Locate every uninfected red blood cell.
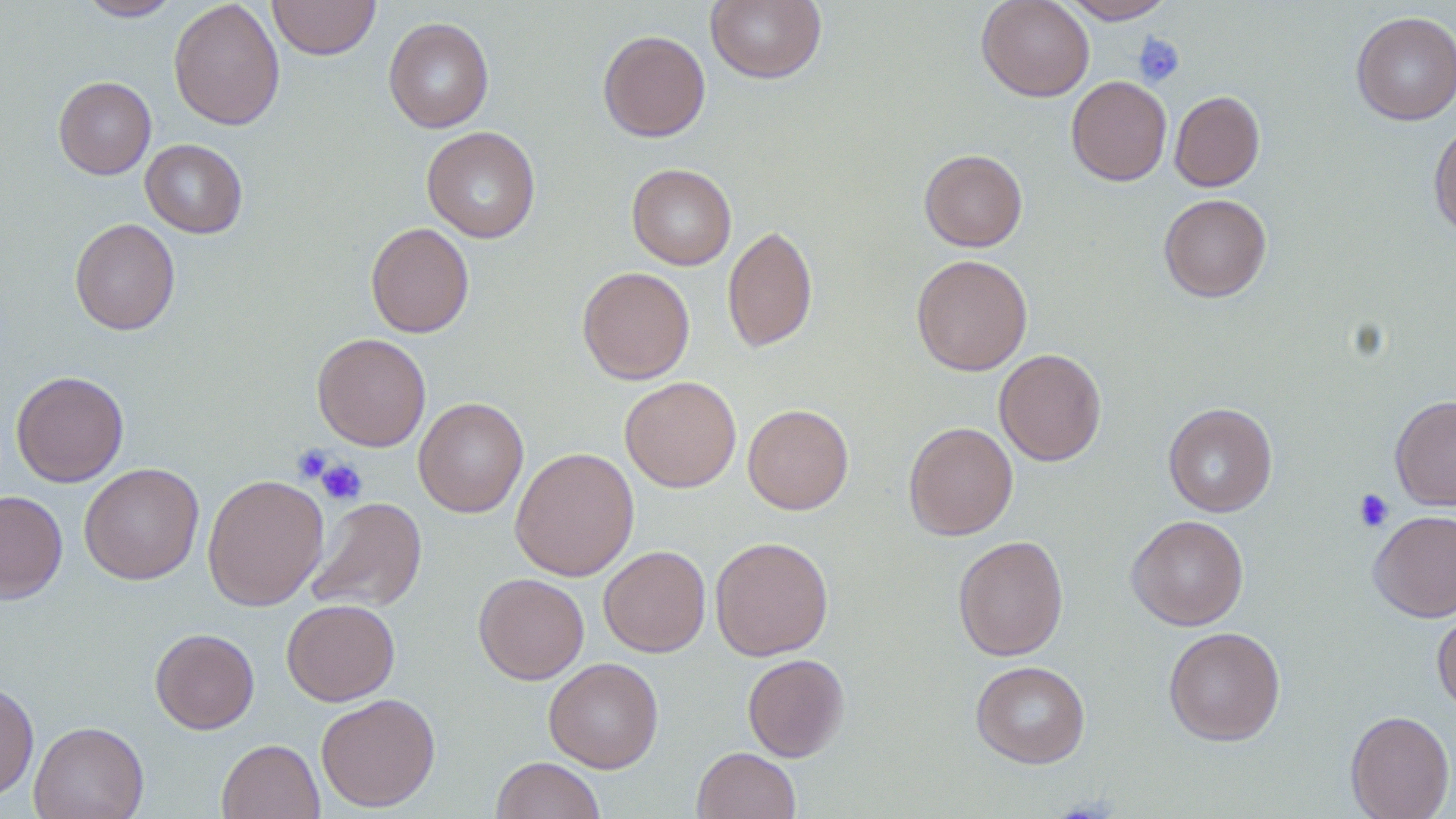
Approximate bounding boxes as [x1, y1, x2, y2] in pixels.
Uninfected red blood cells: [78, 0, 183, 20], [169, 0, 285, 131], [267, 0, 380, 60], [706, 0, 826, 84], [976, 0, 1094, 102], [1061, 0, 1176, 23], [1350, 11, 1456, 125], [383, 16, 494, 133], [597, 29, 711, 142], [53, 76, 156, 179], [1066, 76, 1172, 186], [1169, 90, 1265, 191], [1428, 122, 1456, 239], [422, 126, 540, 243], [140, 139, 248, 238], [919, 149, 1028, 251], [626, 163, 737, 270], [1158, 194, 1272, 302], [69, 218, 180, 335], [365, 222, 475, 338], [723, 224, 818, 353], [911, 253, 1033, 376], [577, 266, 695, 384], [312, 333, 431, 451], [994, 349, 1107, 466], [10, 370, 129, 487], [620, 376, 741, 492], [1389, 395, 1456, 510], [413, 397, 528, 517], [1163, 402, 1277, 517], [743, 404, 854, 515], [903, 422, 1018, 541], [510, 446, 639, 581], [79, 463, 204, 585], [202, 473, 329, 611], [0, 490, 68, 603], [307, 497, 427, 613], [1369, 510, 1456, 622], [1126, 514, 1249, 631], [952, 534, 1069, 661], [710, 536, 834, 661], [598, 545, 711, 657], [473, 573, 589, 684], [281, 599, 400, 706], [1432, 608, 1456, 716], [1163, 626, 1286, 746], [150, 628, 259, 734], [743, 653, 849, 762], [544, 657, 664, 773], [970, 660, 1091, 768], [0, 681, 39, 801], [315, 693, 441, 812], [1345, 710, 1455, 819], [29, 721, 148, 819], [216, 739, 325, 819], [692, 747, 800, 819], [491, 756, 606, 819].

{
  "slide_level_diagnosis": "no evidence of blood parasites",
  "stain": "May-Grünwald-Giemsa",
  "magnification": "1000x",
  "field_of_view": "single",
  "preparation": "thin blood film",
  "modality": "optical microscopy",
  "platelet_locations": "approximate bounding boxes as [x1, y1, x2, y2] in pixels: [1133, 33, 1185, 88], [293, 443, 334, 484], [315, 457, 367, 505], [1353, 488, 1395, 532]",
  "image_size": "1456×819 pixels"
}